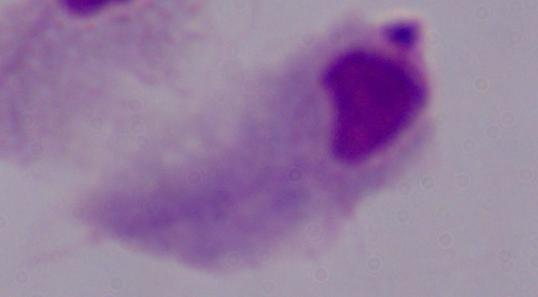

Captured at 1000x magnification. Photomicrograph. A trichomonad is seen.